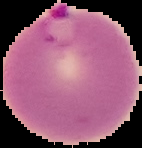

Segmented cell region on a black background. Image is 142×148 pixels. From a thin blood smear. Malaria status: parasitized.